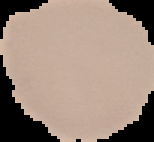 From a thin blood smear. Image is 154×142 pixels. Result: no Plasmodium parasites detected. Cell region segmented out of the field of view; the surrounding area is masked to black.